Assess this cell for malaria.
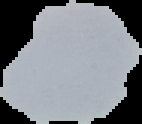

Uninfected.

image size = 142×124 pixels
preparation = thin blood film
image type = segmented cell region with the area outside set to black